Draw a bounding box around every parasitised red blood cell.
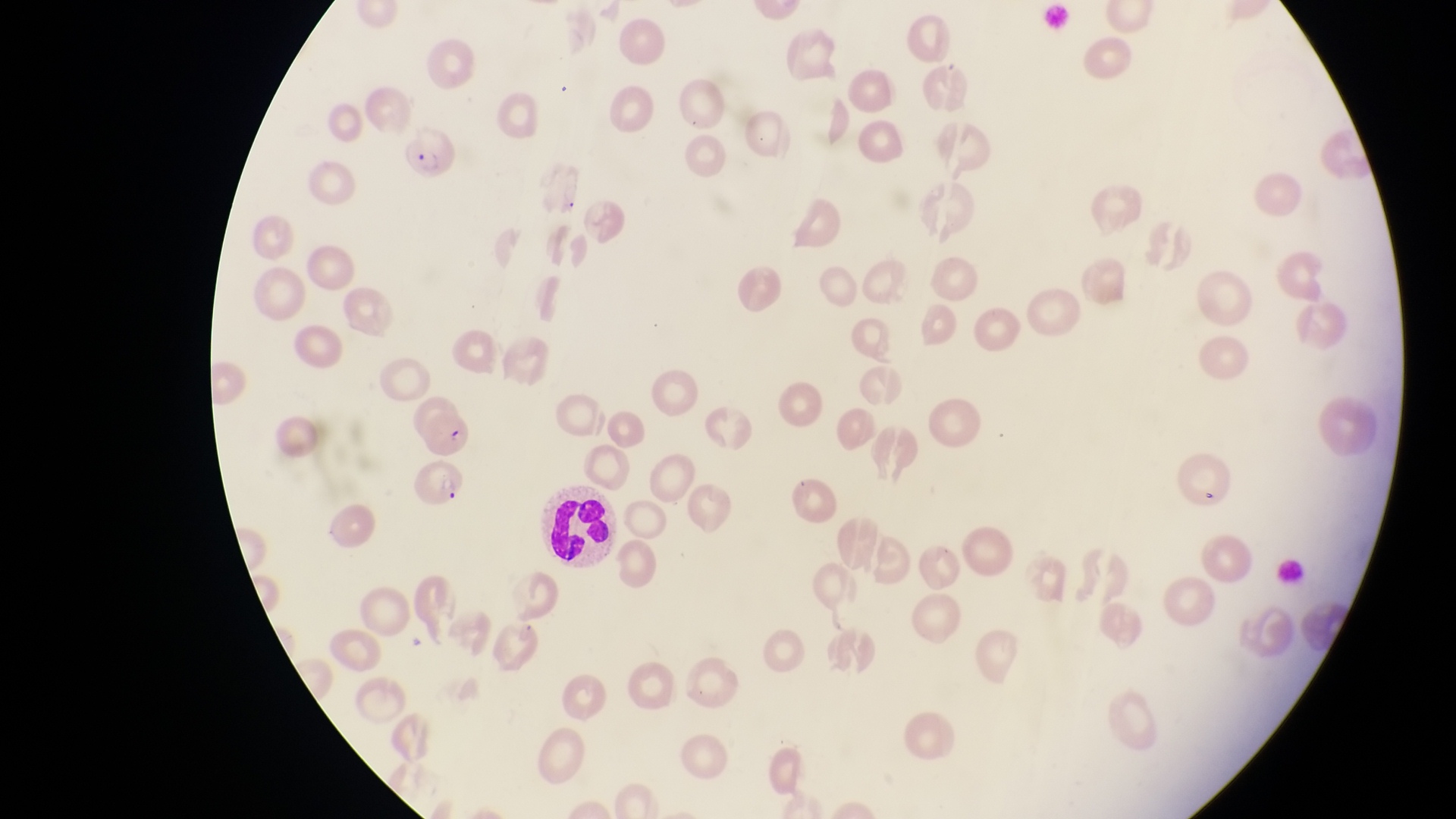
Approximate bounding boxes as left top right bottom in pixels.
Parasitised red blood cells: 403 126 463 185; 416 404 476 451; 406 462 470 511.

Summary:
  - Leukocyte locations: 539 486 621 566
  - Capture: smartphone photograph through the eyepiece of an Olympus CX-23 microscope
  - Country: Uganda
  - Field of view: single
  - Preparation: thin blood smear
  - Magnification: 1000x
  - Image size: 1456×819 pixels